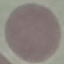

result = no malaria parasites detected
image type = cell patch, automatically extracted from a larger field of view and resized to 64 × 64 pixels
capture = smartphone camera at the microscope eyepiece
stain = Giemsa
preparation = thin blood smear